Identify the preparation type.
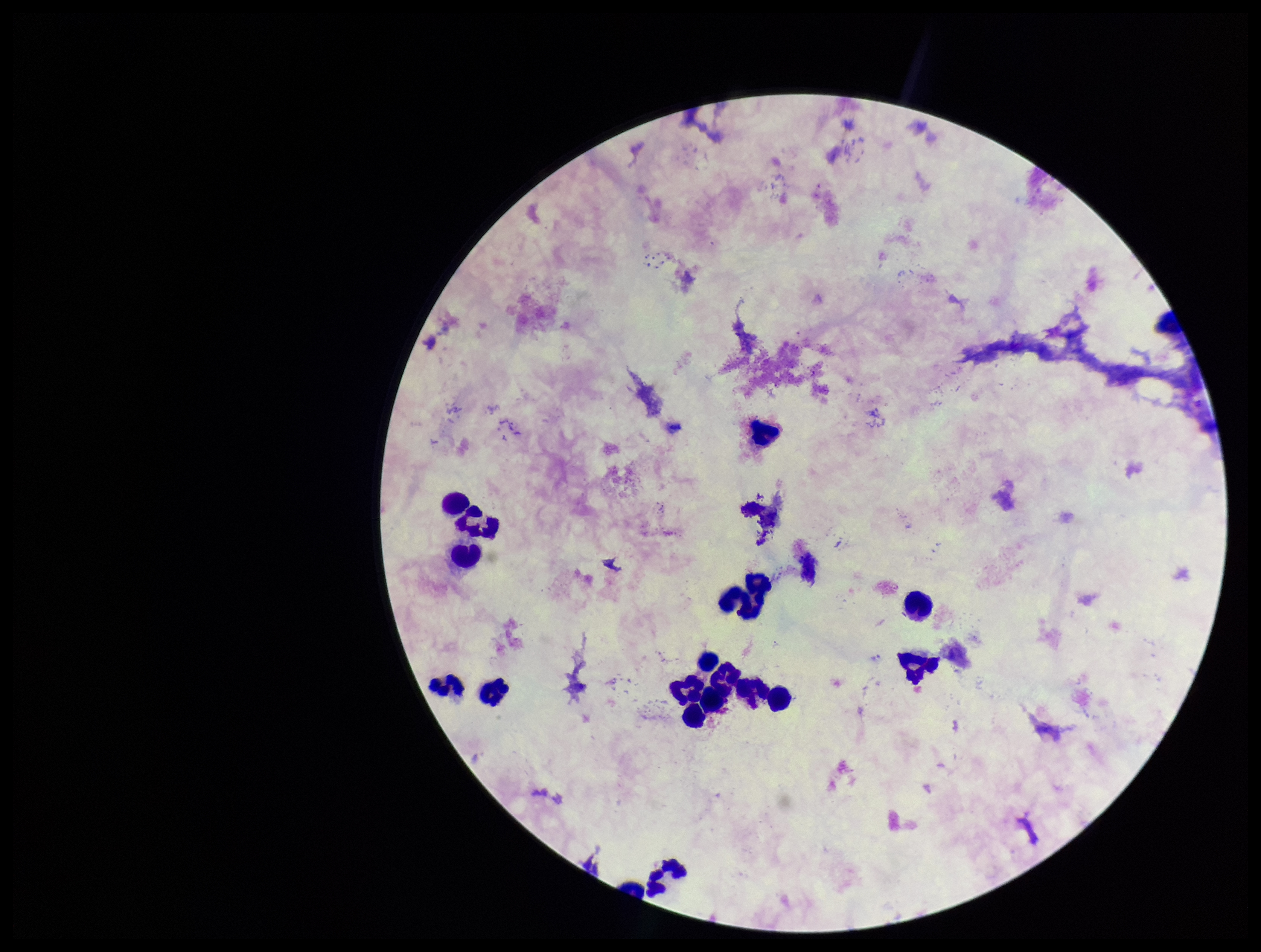

Thick.

{
  "leukocyte_count": 16,
  "image_size": "1261×952 pixels",
  "parasite_count": 0,
  "patient_malaria_status": "negative",
  "capture": "smartphone photograph through the microscope eyepiece",
  "stain": "Giemsa",
  "plasmodium_parasites": "none seen",
  "field_of_view": "one from this slide"
}